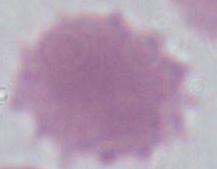

Summary:
  - Modality: micrograph
  - Magnification: 1000x
  - Identification: erythrocyte